Assess this cell for malaria.
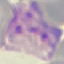

It is parasitized.

Summary:
  - Image type: automatically extracted cell patch, resized to 64 × 64 pixels
  - Preparation: thin blood smear
  - Capture: smartphone camera at the microscope eyepiece
  - Stain: Giemsa